Classify this cell by malaria status.
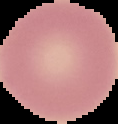

It is uninfected.

Image is 118×124 pixels. The area outside the segmented cell region is set to black. From a thin blood smear.